Report the malaria status of this cell.
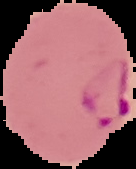

Parasitized.

Segmented cell region on a black background. Image is 136×169 pixels. From a thin blood smear.